Name the cell type shown.
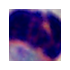

This is a leukocyte.

1000x magnification. Photomicrograph.